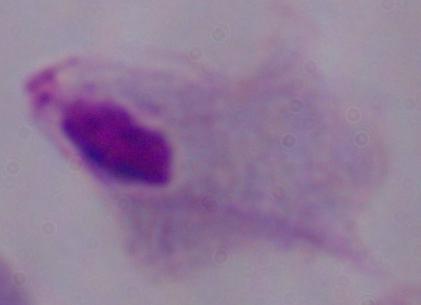
magnification = 1000x
modality = micrograph
identification = trichomonad